Outline each blood parasite and name the species.
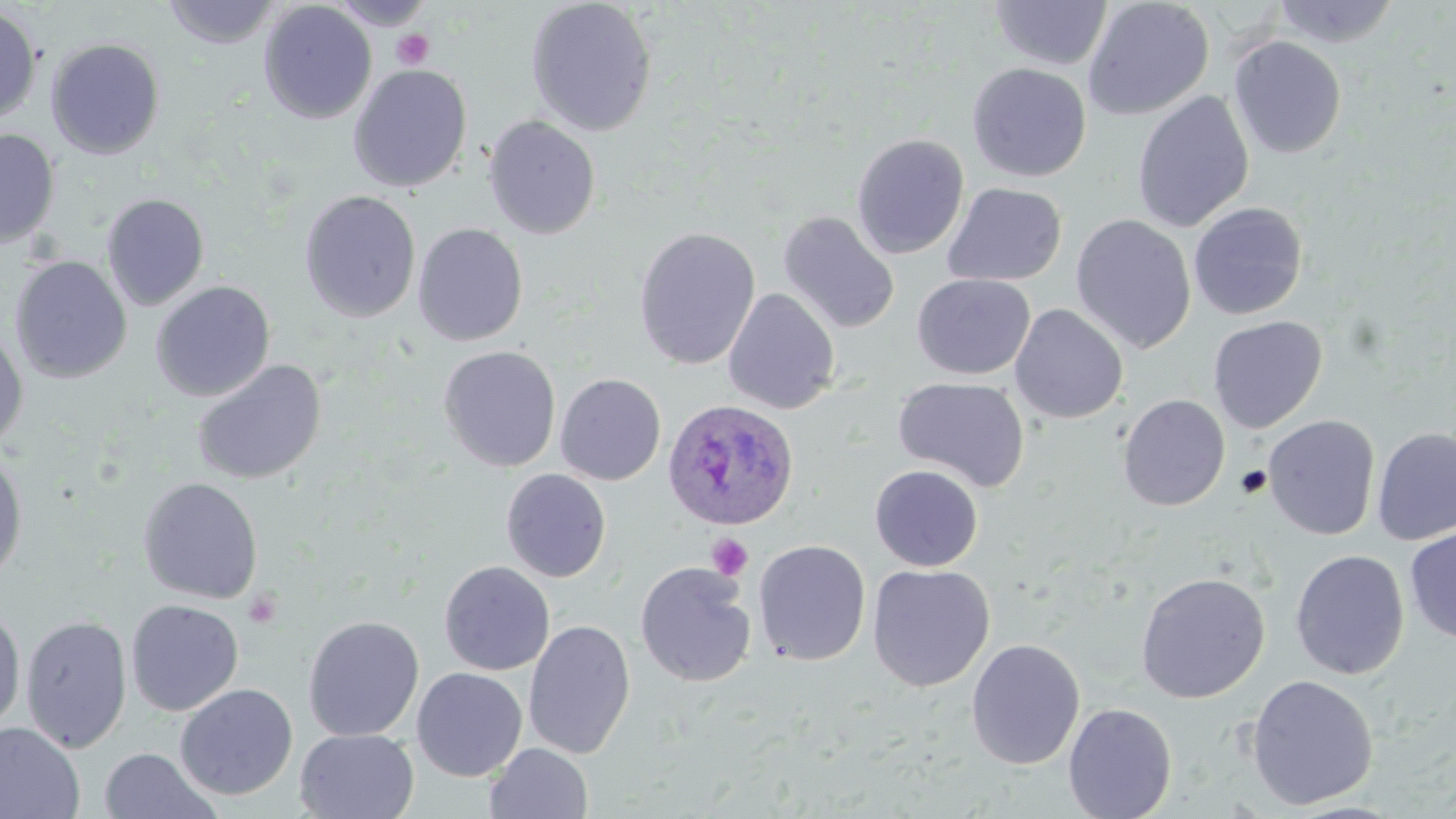
Approximate bounding boxes as (x1,y1)-(x2,y2) corner pairs in pixels.
Plasmodium ovale-infected red blood cells: (661,398)-(800,531).
No Plasmodium falciparum, Plasmodium malariae, Plasmodium vivax, Babesia divergens, or Trypanosoma brucei observed.

Summary:
  - Uninfected red blood cell locations: (326,0)-(437,30), (525,0)-(659,137), (1082,0)-(1214,121), (163,1)-(281,49), (988,1)-(1113,70), (1271,1)-(1401,48), (258,2)-(377,124), (0,5)-(42,126), (1228,36)-(1347,159), (46,38)-(165,158), (967,62)-(1092,182), (348,64)-(472,193), (1132,90)-(1255,233), (483,115)-(601,240), (0,129)-(60,249), (851,133)-(969,259), (943,182)-(1067,287), (299,190)-(421,323), (101,193)-(210,311), (1187,202)-(1309,321), (777,211)-(900,335), (1070,214)-(1196,355), (411,223)-(528,346), (633,226)-(761,370), (10,256)-(132,383), (912,273)-(1035,380), (151,280)-(275,402), (722,288)-(841,415), (1009,304)-(1128,424), (1207,315)-(1328,433), (0,325)-(28,452), (438,345)-(561,472), (191,360)-(327,485), (555,373)-(666,485), (893,376)-(1030,492), (1117,394)-(1230,511), (1263,414)-(1381,540), (1372,426)-(1456,546), (0,451)-(28,583), (869,464)-(984,571), (500,468)-(612,582), (137,477)-(264,604), (1404,525)-(1456,645), (753,539)-(871,666), (1290,549)-(1410,680), (439,560)-(555,675), (635,562)-(757,688), (867,563)-(995,692), (1135,571)-(1270,703), (126,599)-(244,716), (0,605)-(26,732), (21,615)-(132,755), (303,615)-(424,741), (523,619)-(636,760), (966,638)-(1085,770), (411,667)-(528,781), (1246,674)-(1379,809), (174,683)-(298,800), (1063,703)-(1177,819), (0,722)-(84,819), (295,728)-(420,819), (485,742)-(593,819), (98,747)-(222,819)
  - Platelet locations: (391,29)-(434,70), (1235,465)-(1273,499), (707,532)-(753,581), (243,590)-(282,629)
  - Slide-level diagnosis: Plasmodium ovale
  - Image size: 1456×819 pixels
  - Modality: optical microscopy
  - Preparation: thin blood smear
  - Stain: May-Grünwald-Giemsa
  - Field of view: single
  - Magnification: 1000x